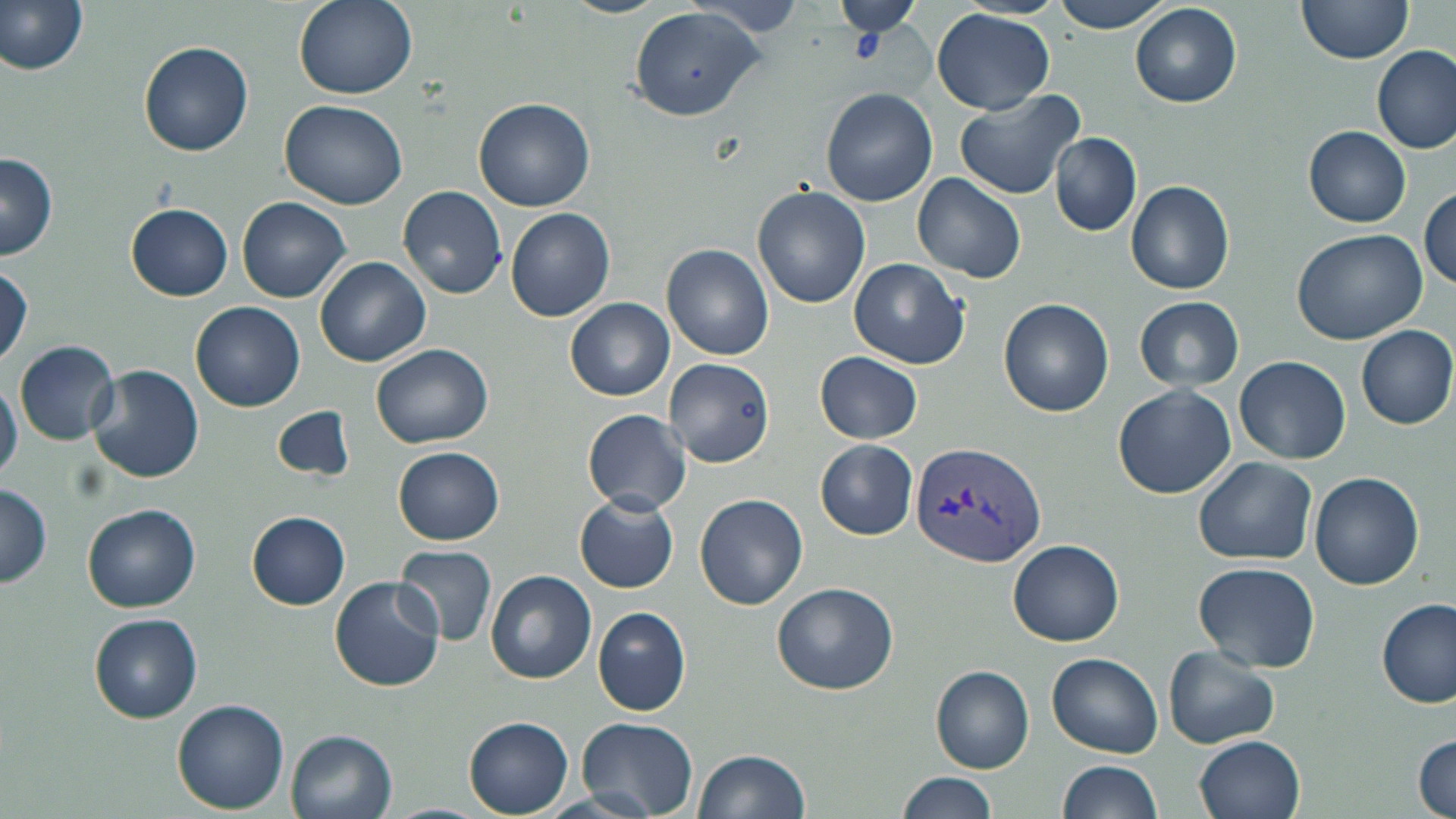
Summary:
  - Coordinate format: approximate bounding boxes as [x1, y1, x2, y2] in pixels
  - Platelet locations: [851, 31, 886, 64]
  - Plasmodium vivax-infected red blood cell locations: [909, 440, 1048, 571]
  - Uninfected red blood cell locations: [0, 0, 89, 76], [294, 0, 417, 100], [559, 0, 670, 18], [836, 0, 920, 40], [1051, 0, 1174, 34], [686, 1, 809, 41], [1295, 1, 1415, 68], [1132, 5, 1242, 108], [626, 7, 767, 122], [932, 7, 1056, 114], [137, 40, 253, 157], [1372, 44, 1455, 153], [820, 88, 938, 206], [954, 88, 1085, 201], [474, 97, 597, 212], [280, 100, 407, 209], [1305, 127, 1411, 227], [1051, 133, 1142, 235], [0, 153, 59, 259], [913, 173, 1027, 283], [1125, 180, 1235, 294], [398, 184, 508, 299], [752, 186, 869, 309], [1418, 188, 1455, 292], [238, 197, 350, 303], [124, 202, 233, 299], [507, 208, 616, 322], [1292, 229, 1426, 345], [663, 244, 773, 362], [315, 256, 430, 366], [848, 257, 971, 369], [0, 264, 32, 366], [1135, 296, 1244, 391], [566, 297, 675, 401], [999, 299, 1115, 417], [192, 301, 305, 412], [1356, 325, 1456, 429], [15, 340, 118, 443], [372, 343, 493, 448], [816, 352, 921, 444], [1235, 356, 1350, 464], [663, 358, 774, 465], [88, 362, 205, 484], [0, 376, 21, 483], [1112, 385, 1236, 499], [273, 406, 354, 481], [584, 408, 691, 514], [816, 439, 918, 540], [394, 446, 505, 544], [1193, 456, 1317, 566], [1309, 472, 1426, 590], [0, 483, 53, 588], [573, 492, 679, 592], [695, 494, 809, 609], [581, 500, 678, 702], [82, 503, 201, 612], [246, 512, 351, 609], [1009, 540, 1124, 646], [395, 545, 498, 647], [1193, 561, 1320, 673], [485, 570, 596, 683], [330, 575, 445, 692], [771, 581, 897, 696], [1378, 599, 1455, 708], [593, 607, 692, 718], [89, 612, 202, 723], [1163, 647, 1280, 748], [1046, 652, 1164, 758], [931, 665, 1036, 772], [172, 698, 289, 813], [463, 716, 574, 815], [577, 716, 699, 816], [285, 729, 398, 819], [1414, 734, 1455, 818], [1194, 736, 1304, 819], [693, 748, 810, 818], [1060, 760, 1164, 818], [896, 772, 1002, 819], [533, 791, 661, 819], [376, 803, 490, 819]
  - Slide-level diagnosis: Plasmodium vivax
  - Preparation: thin blood smear
  - Field of view: single
  - Stain: May-Grünwald-Giemsa
  - Magnification: 1000x
  - Modality: optical microscopy
  - Image size: 1456×819 pixels